State the blood parasite species.
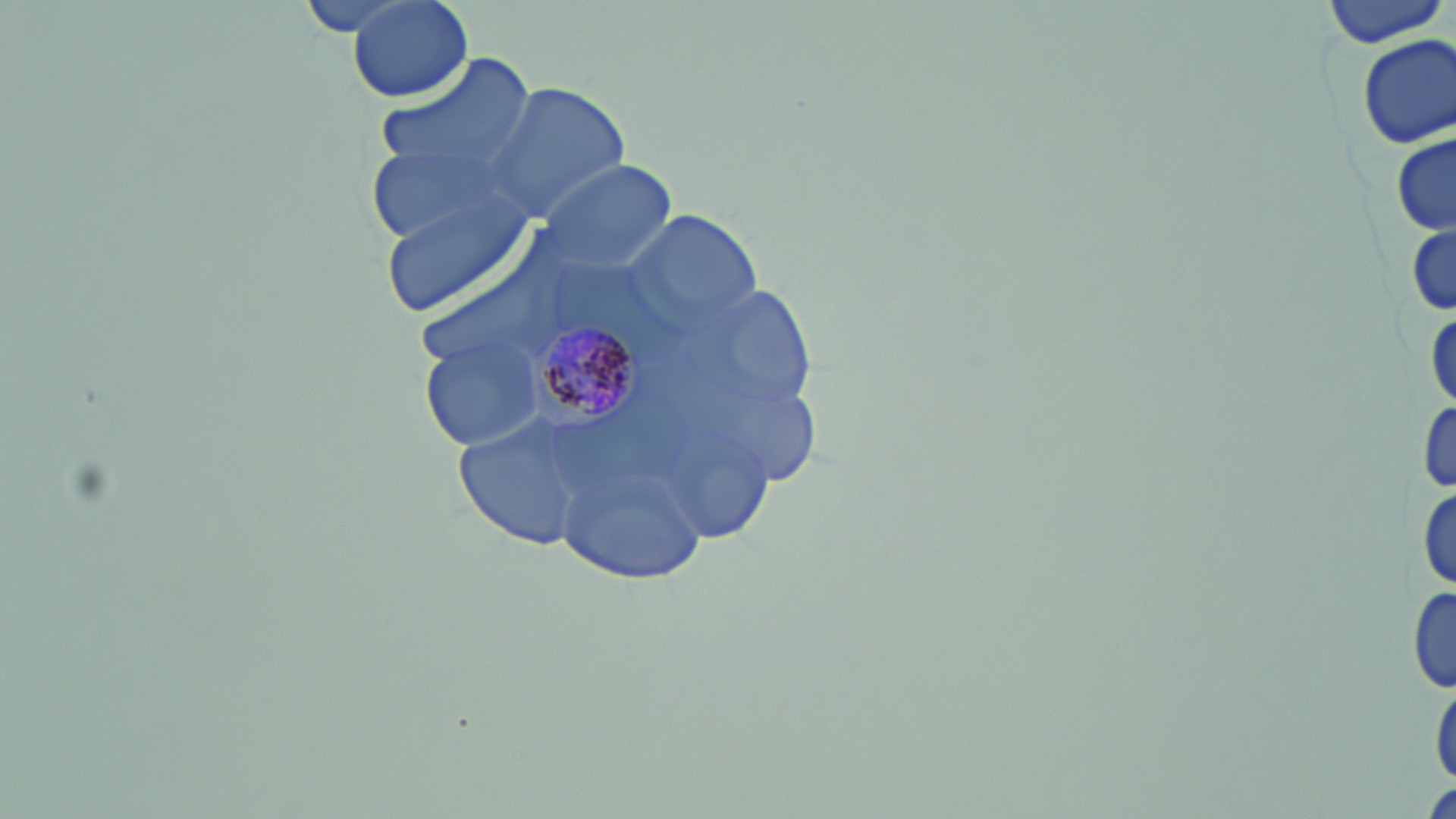

Plasmodium malariae.

Approximate bounding boxes as (x1, y1, x2, y2) in pixels. Plasmodium malariae-infected red blood cell locations: (537, 317, 639, 422). Uninfected red blood cell locations: (294, 0, 422, 39), (345, 0, 477, 104), (1319, 0, 1448, 48), (1356, 34, 1454, 150), (370, 56, 536, 190), (485, 81, 630, 224), (1392, 133, 1455, 235), (536, 160, 678, 273), (375, 186, 538, 321), (630, 213, 764, 333), (1407, 222, 1455, 319), (419, 334, 546, 451), (1418, 399, 1456, 495), (450, 414, 600, 551), (556, 463, 707, 581), (1414, 478, 1456, 595), (1408, 582, 1455, 696), (1432, 673, 1456, 791), (1423, 778, 1456, 819). Optical microscopy. Thin blood smear. Single field of view. Image is 1456×819 pixels. May-Grünwald-Giemsa-stained preparation. 1000x magnification.